Assess the morphology of the erythrocytes.
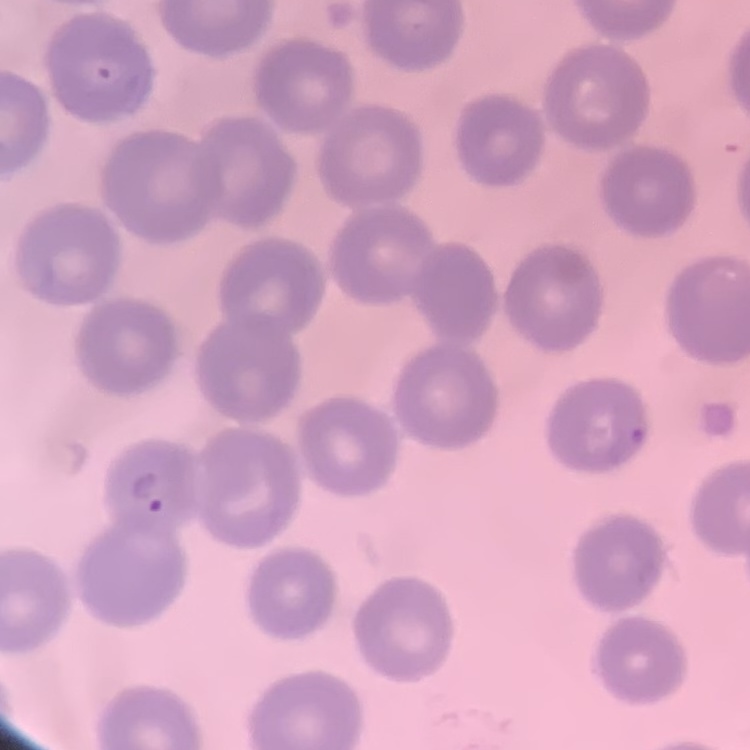
No rouleaux formation.

Field's or Giemsa stain. Thin blood film. Square crop of a larger photomicrograph.